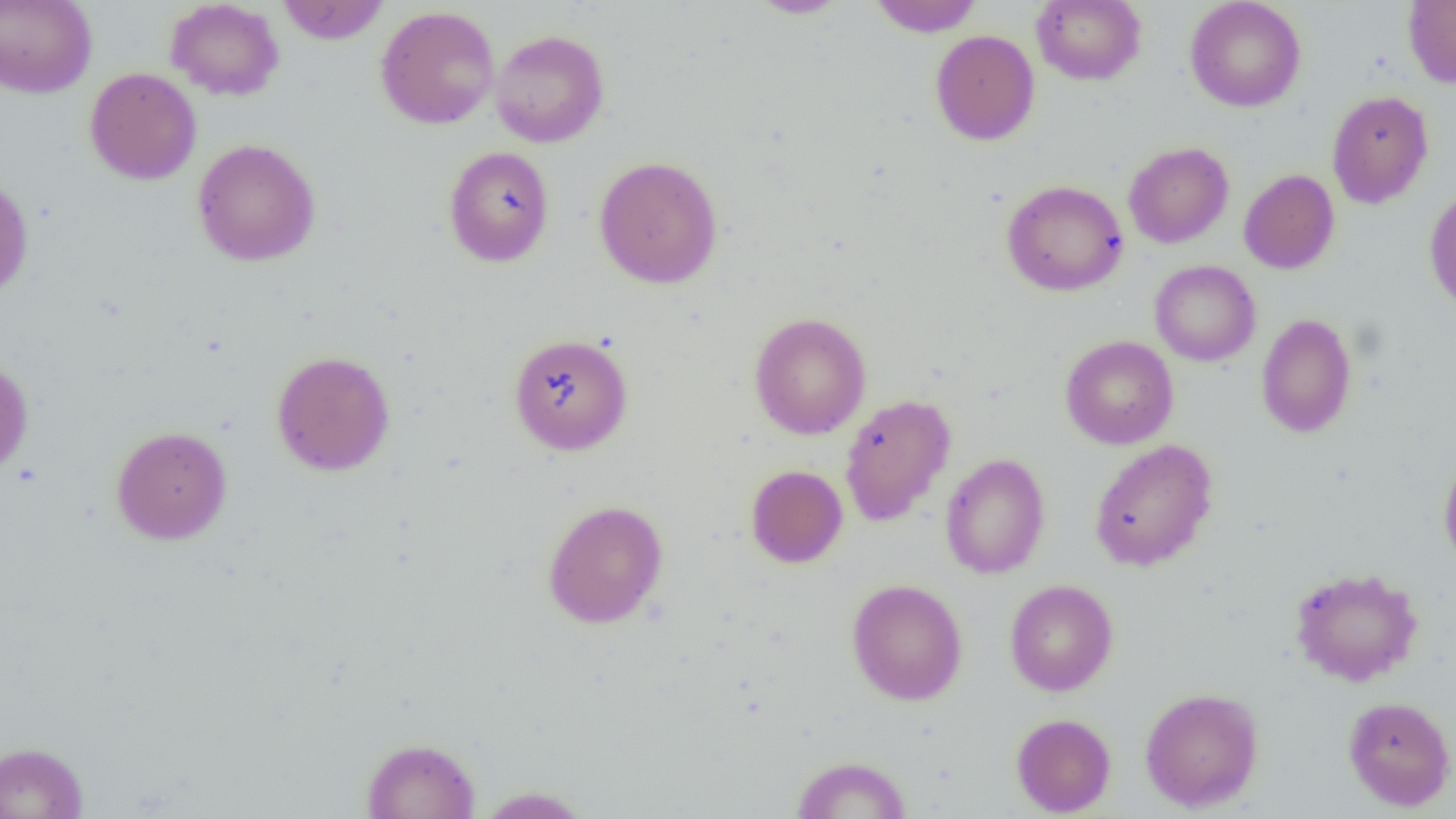 Approximate bounding boxes as [x1, y1, x2, y2] in pixels. Uninfected red blood cell locations: [165, 0, 285, 101], [276, 0, 390, 44], [747, 0, 851, 18], [868, 0, 983, 36], [1032, 0, 1146, 85], [1185, 0, 1306, 112], [0, 1, 97, 98], [1403, 1, 1456, 88], [375, 5, 500, 129], [490, 29, 609, 147], [930, 29, 1040, 145], [84, 67, 202, 185], [1326, 90, 1434, 208], [192, 138, 321, 267], [1123, 142, 1234, 248], [443, 146, 555, 267], [593, 155, 723, 289], [1239, 169, 1339, 274], [0, 174, 34, 302], [1001, 179, 1128, 296], [1423, 186, 1456, 314], [1149, 260, 1261, 366], [748, 311, 871, 439], [1256, 313, 1357, 438], [507, 332, 634, 455], [1060, 335, 1178, 449], [271, 350, 396, 475], [0, 359, 33, 479], [840, 394, 956, 526], [111, 425, 232, 545], [1089, 439, 1218, 571], [1438, 450, 1456, 575], [939, 453, 1050, 578], [745, 465, 848, 568], [542, 499, 669, 629], [1289, 566, 1424, 686], [847, 578, 968, 705], [1004, 579, 1118, 696], [1140, 687, 1264, 812], [1343, 695, 1456, 811], [1011, 713, 1116, 817], [361, 737, 480, 818], [0, 742, 89, 819], [791, 755, 911, 818], [474, 786, 593, 818]. Slide-level diagnosis: no evidence of blood parasites. Image is 1456×819 pixels. Single field of view. Optical microscopy. Captured at 1000x magnification. Thin blood smear.